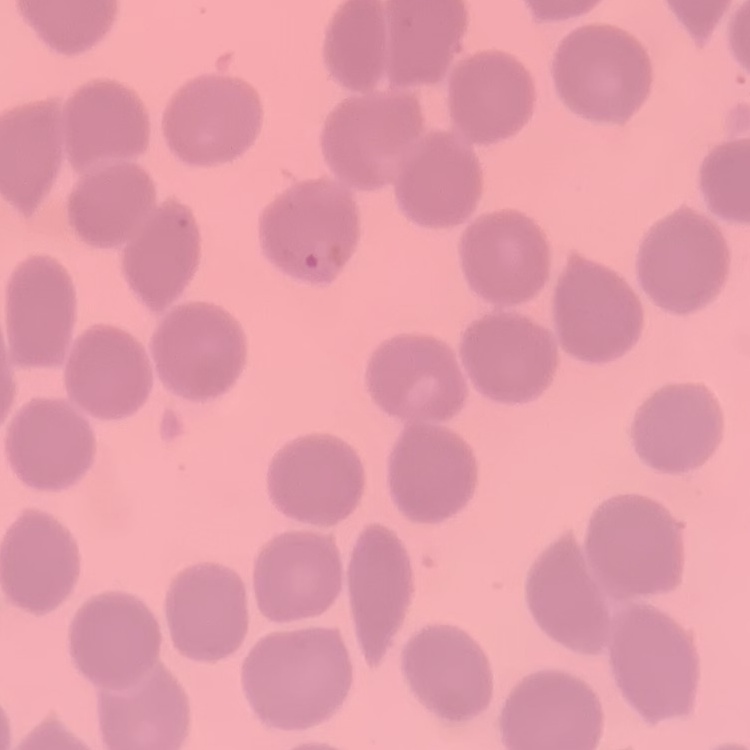
The erythrocytes exhibit no rouleaux formation. Stained with either Field's or Giemsa. Square crop of a larger photomicrograph. Thin blood smear.